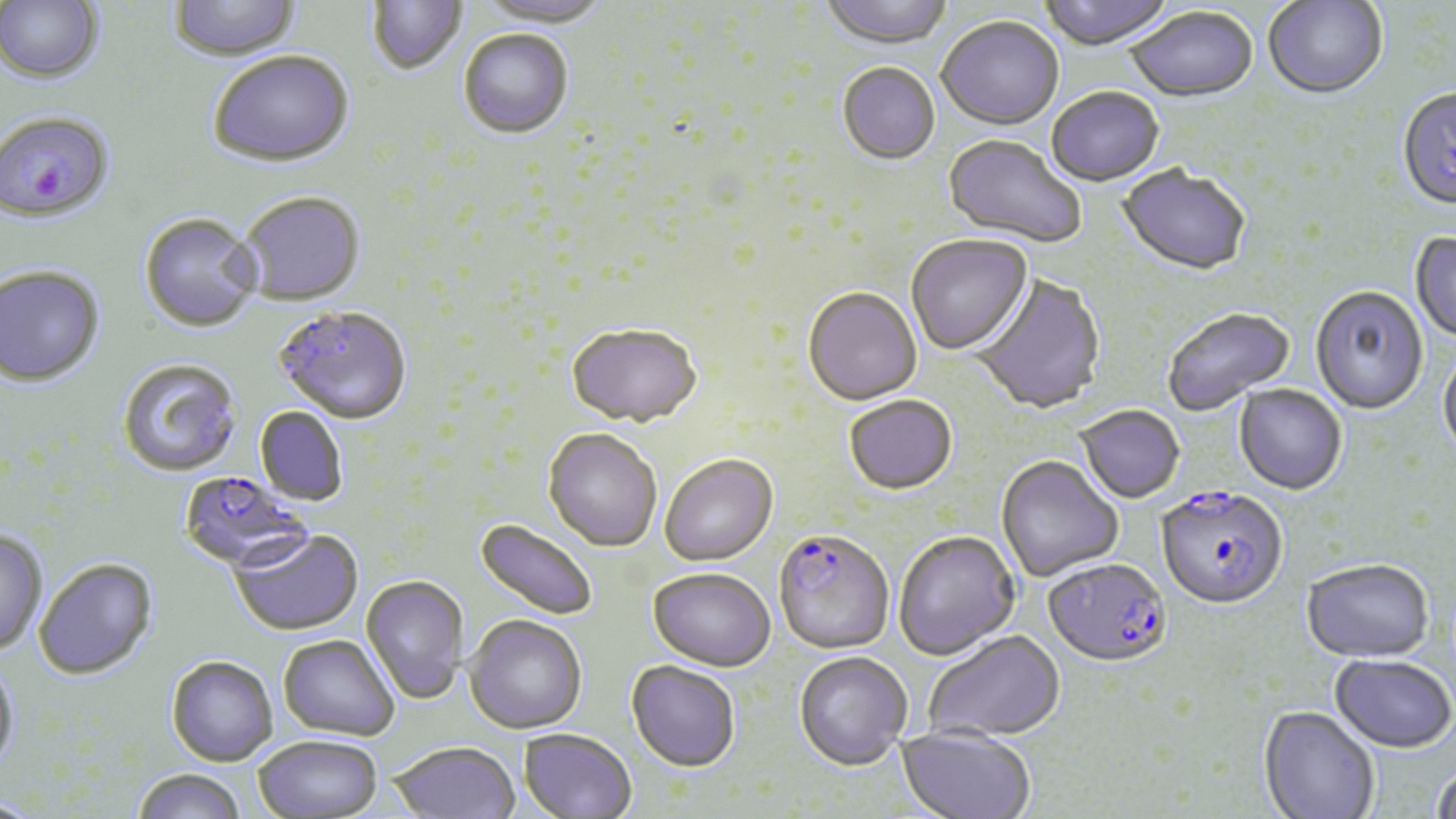
Approximate bounding boxes as (x1,y1)-(x2,y2) corner pairs in pixels. Plasmodium falciparum-infected red blood cell locations: (0,110)-(116,224), (177,471)-(314,573), (1156,488)-(1288,612), (772,529)-(896,655), (1043,560)-(1173,671). Uninfected red blood cell locations: (168,0)-(303,63), (476,0)-(610,30), (818,0)-(955,52), (1037,0)-(1176,52), (0,1)-(103,83), (367,1)-(467,76), (1263,1)-(1388,102), (1125,9)-(1259,106), (936,18)-(1064,132), (458,31)-(573,140), (209,53)-(354,169), (837,64)-(940,166), (1047,89)-(1164,188), (1396,89)-(1456,213), (941,135)-(1085,250), (1116,166)-(1251,278), (239,193)-(366,307), (138,214)-(264,334), (1410,232)-(1456,346), (906,235)-(1033,357), (0,266)-(105,389), (972,273)-(1106,416), (1310,288)-(1428,417), (803,289)-(922,407), (274,306)-(413,424), (1163,308)-(1295,416), (567,325)-(702,428), (1437,352)-(1456,463), (117,359)-(242,478), (1233,385)-(1347,497), (844,396)-(957,495), (255,406)-(349,507), (1075,407)-(1184,506), (543,427)-(663,551), (660,454)-(778,565), (995,457)-(1124,582), (475,518)-(599,621), (229,529)-(364,636), (0,530)-(48,656), (893,531)-(1021,661), (34,559)-(158,681), (1301,561)-(1435,665), (648,568)-(776,671), (361,575)-(470,703), (464,614)-(588,734), (924,631)-(1065,743), (278,635)-(399,741), (794,652)-(912,771), (1329,655)-(1455,755), (166,656)-(278,766), (0,660)-(20,775), (626,660)-(741,772), (1258,706)-(1380,819), (896,725)-(1035,819), (518,728)-(637,819), (254,735)-(383,817), (388,741)-(520,819), (1431,768)-(1456,819), (131,769)-(247,819). Slide-level diagnosis: Plasmodium falciparum. Captured at 1000x magnification. Thin blood smear. May-Grünwald-Giemsa stain. Optical microscopy. Image is 1456×819 pixels. One field of a larger specimen.